Give the extent of all uninfected red blood cells.
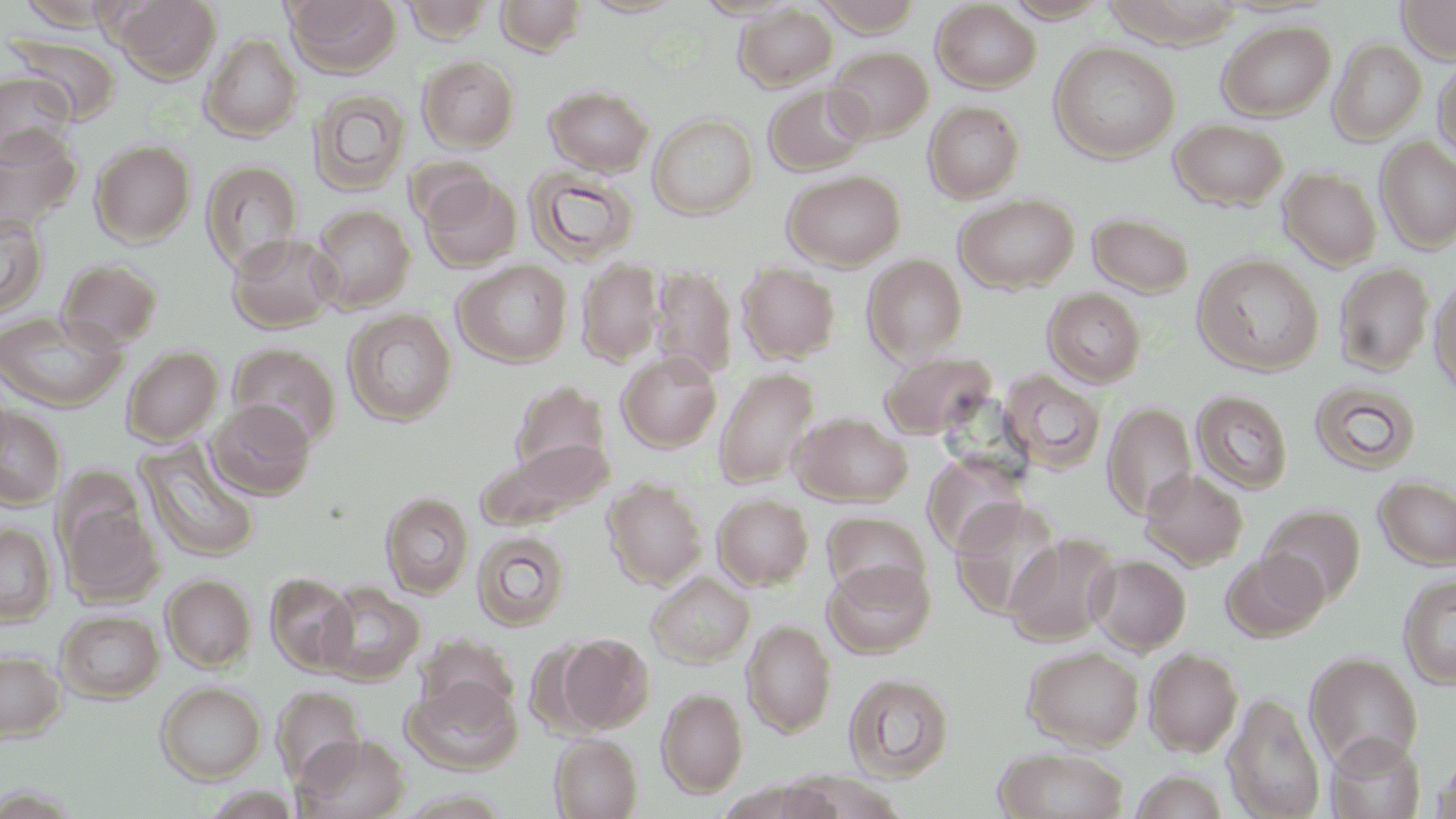
Approximate bounding boxes as (x1, y1, x2, y2) in pixels.
Uninfected red blood cells: (115, 0, 220, 83), (284, 0, 401, 77), (402, 0, 494, 43), (495, 0, 587, 56), (692, 0, 799, 20), (812, 0, 926, 36), (1002, 0, 1111, 22), (1397, 0, 1456, 64), (15, 1, 123, 29), (580, 1, 685, 18), (931, 2, 1041, 92), (734, 4, 837, 91), (1217, 19, 1336, 120), (6, 33, 123, 123), (201, 34, 303, 140), (1328, 38, 1427, 144), (1049, 41, 1180, 162), (826, 46, 933, 142), (418, 55, 520, 152), (1432, 57, 1456, 164), (0, 71, 75, 162), (545, 85, 654, 175), (763, 85, 871, 175), (308, 88, 410, 196), (924, 101, 1024, 202), (648, 114, 758, 219), (1169, 118, 1289, 210), (0, 127, 82, 230), (1375, 137, 1456, 252), (90, 140, 196, 246), (201, 161, 303, 272), (523, 166, 639, 264), (1279, 167, 1382, 270), (782, 170, 905, 271), (419, 174, 523, 272), (954, 194, 1079, 293), (309, 204, 415, 312), (1087, 211, 1195, 297), (0, 213, 49, 318), (227, 232, 341, 334), (862, 253, 968, 363), (1192, 253, 1324, 375), (56, 258, 164, 351), (577, 259, 664, 365), (454, 260, 572, 367), (737, 263, 840, 363), (1334, 263, 1434, 375), (652, 266, 737, 381), (1429, 276, 1456, 399), (1043, 288, 1146, 387), (343, 309, 457, 426), (0, 311, 126, 412), (228, 343, 341, 449), (122, 345, 223, 446), (617, 351, 722, 452), (880, 352, 997, 439), (714, 367, 819, 488), (999, 370, 1107, 472), (510, 379, 614, 485), (1309, 381, 1421, 475), (1191, 390, 1293, 493), (207, 399, 316, 499), (1103, 401, 1198, 519), (0, 406, 67, 509), (794, 412, 912, 505), (136, 438, 261, 563), (482, 441, 614, 525), (923, 452, 1027, 555), (1139, 469, 1248, 569), (1373, 476, 1456, 569), (604, 477, 707, 588), (381, 492, 474, 598), (713, 493, 814, 589), (950, 498, 1062, 618), (60, 499, 162, 605), (1259, 504, 1365, 604), (823, 511, 930, 603), (0, 522, 56, 625), (472, 530, 571, 631), (1005, 532, 1120, 645), (1222, 550, 1328, 641), (1088, 553, 1191, 654), (824, 559, 934, 657), (647, 571, 754, 667), (265, 573, 358, 675), (161, 574, 256, 671), (1398, 574, 1456, 688), (318, 582, 425, 684), (56, 610, 164, 702), (742, 620, 837, 736), (557, 634, 654, 733), (1022, 645, 1144, 751), (1143, 647, 1243, 756), (0, 649, 65, 741), (1304, 652, 1422, 771), (843, 672, 955, 781), (402, 676, 523, 774), (156, 681, 266, 783), (272, 686, 367, 786), (657, 687, 748, 797), (1224, 693, 1326, 819), (293, 733, 410, 819), (1323, 733, 1426, 819), (551, 735, 642, 818), (994, 747, 1129, 819), (1433, 752, 1456, 819), (1127, 769, 1231, 818), (783, 773, 902, 817).

Summary:
  - Slide-level diagnosis: no evidence of blood parasites
  - Image size: 1456×819 pixels
  - Magnification: 1000x
  - Field of view: single
  - Stain: May-Grünwald-Giemsa
  - Modality: optical microscopy
  - Preparation: thin blood smear